Locate and identify every blood parasite.
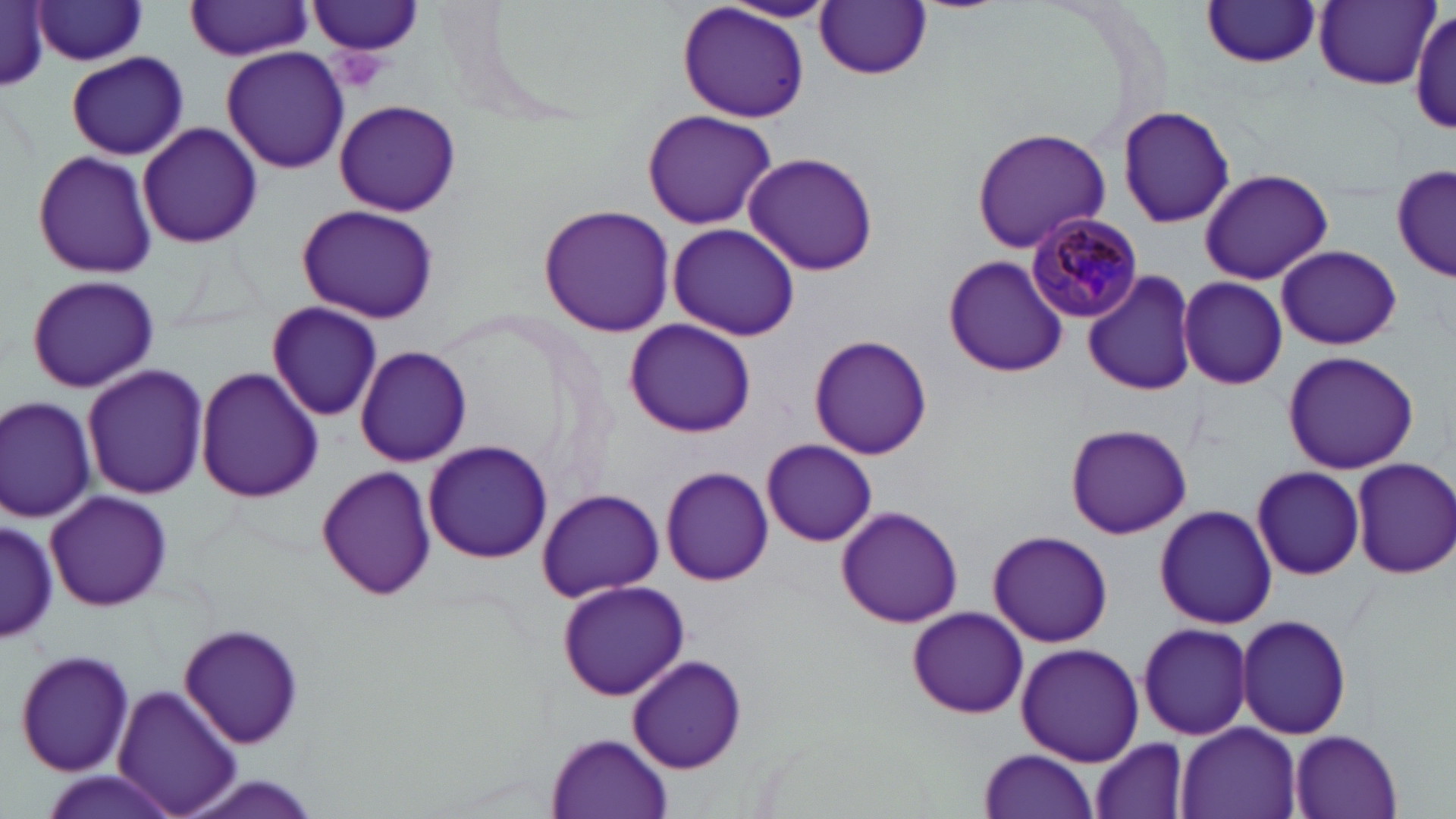

Approximate bounding boxes as (x1, y1, x2, y2) in pixels.
Plasmodium malariae-infected red blood cells: (1027, 212, 1142, 325).
No Plasmodium falciparum, Plasmodium ovale, Plasmodium vivax, Babesia divergens, or Trypanosoma brucei observed.

Summary:
  - Platelet locations: (330, 45, 389, 90)
  - Uninfected red blood cell locations: (186, 1, 315, 60), (308, 1, 427, 60), (675, 1, 811, 124), (720, 1, 840, 23), (1202, 1, 1323, 70), (1314, 1, 1440, 89), (816, 2, 932, 80), (1, 3, 52, 93), (31, 3, 150, 67), (1413, 7, 1454, 137), (220, 46, 350, 175), (67, 52, 187, 160), (331, 98, 464, 215), (1116, 103, 1237, 229), (642, 108, 777, 231), (136, 121, 263, 250), (970, 128, 1112, 252), (31, 148, 158, 281), (743, 152, 883, 277), (1394, 165, 1456, 279), (1197, 169, 1333, 285), (294, 203, 441, 324), (538, 203, 676, 338), (667, 224, 801, 341), (1276, 244, 1401, 350), (943, 253, 1068, 379), (1082, 271, 1200, 396), (25, 274, 159, 393), (1178, 276, 1287, 389), (267, 300, 382, 422), (624, 319, 757, 439), (808, 334, 933, 461), (354, 345, 474, 467), (1282, 350, 1420, 475), (81, 363, 210, 501), (195, 367, 324, 504), (1, 395, 99, 522), (1066, 424, 1194, 538), (762, 438, 879, 546), (423, 441, 552, 564), (1352, 459, 1456, 578), (314, 463, 438, 602), (1251, 465, 1366, 580), (659, 466, 771, 586), (45, 488, 173, 613), (537, 488, 663, 603), (1153, 504, 1277, 628), (835, 506, 961, 627), (1, 519, 59, 644), (987, 530, 1113, 647), (556, 578, 690, 701), (907, 607, 1027, 718), (1237, 613, 1353, 740), (1137, 621, 1252, 741), (179, 622, 305, 752), (1016, 642, 1144, 765), (14, 646, 137, 779), (628, 653, 747, 775), (112, 683, 241, 816), (1175, 723, 1300, 819), (1289, 730, 1402, 819), (547, 732, 672, 817), (1089, 736, 1192, 819), (977, 748, 1100, 819)
  - Slide-level diagnosis: Plasmodium malariae
  - Magnification: 1000x
  - Field of view: one of a larger specimen
  - Image size: 1456×819 pixels
  - Stain: May-Grünwald-Giemsa
  - Modality: optical microscopy
  - Preparation: thin blood film